State which parasite is depicted.
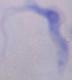
This is a trypanosome.

Summary:
  - Magnification: 1000x
  - Modality: micrograph